Comment on the morphology of the erythrocytes.
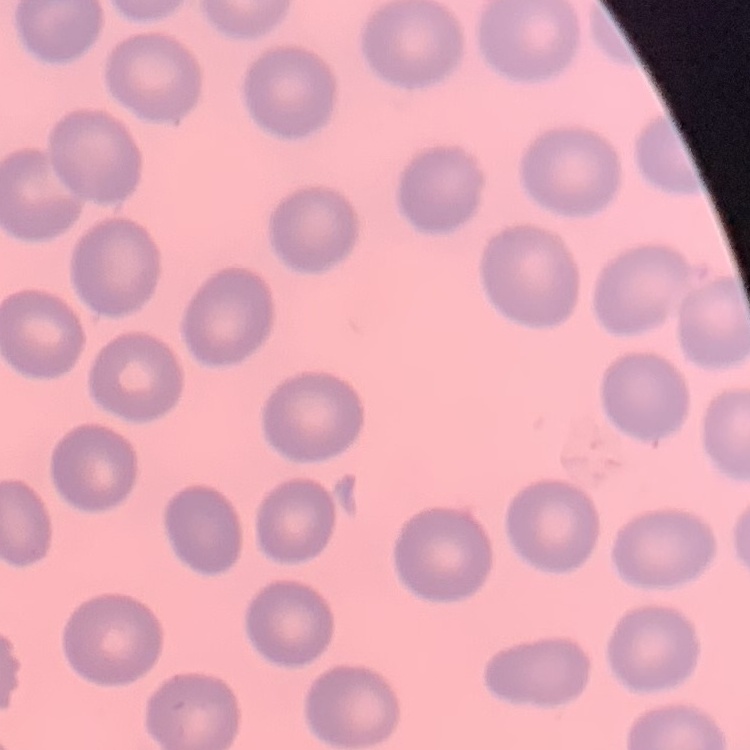
They show no rouleaux formation.

Stained with either Field's or Giemsa. Thin peripheral smear. Square crop of a larger photomicrograph.